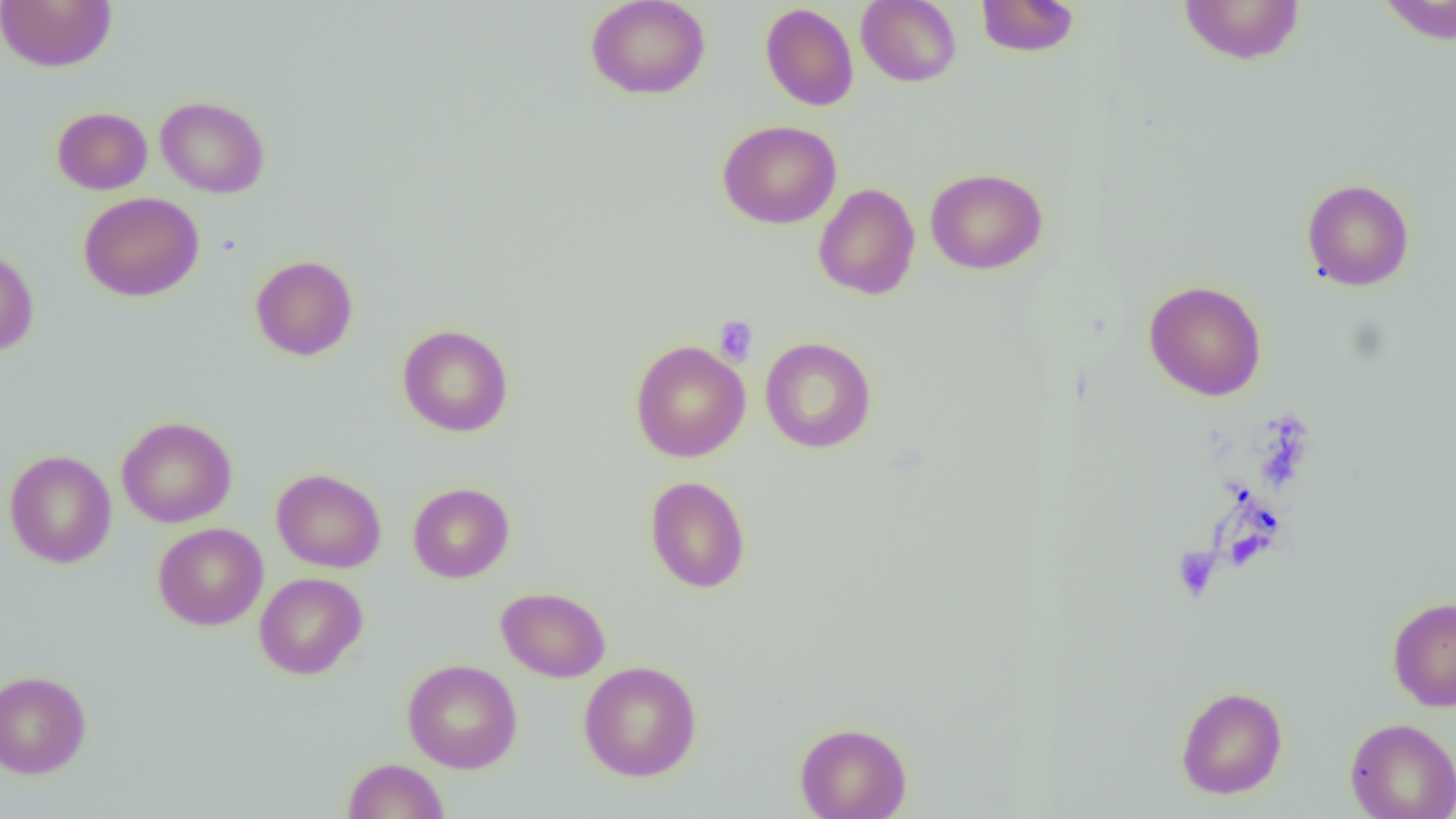 Approximate bounding boxes as (x1, y1, x2, y2) in pixels. Uninfected red blood cell locations: (0, 0, 117, 72), (585, 0, 711, 99), (857, 0, 961, 87), (975, 0, 1081, 57), (1178, 0, 1306, 65), (1376, 1, 1456, 44), (760, 3, 859, 111), (156, 96, 270, 198), (52, 107, 152, 195), (717, 120, 842, 229), (925, 167, 1048, 275), (1302, 178, 1414, 291), (814, 183, 920, 300), (78, 192, 204, 302), (0, 245, 40, 356), (250, 255, 358, 361), (1143, 280, 1267, 401), (397, 323, 514, 437), (759, 336, 876, 453), (630, 339, 750, 462), (116, 416, 237, 528), (4, 450, 117, 568), (271, 468, 386, 573), (645, 476, 751, 593), (407, 482, 515, 583), (153, 523, 268, 630), (254, 572, 367, 679), (496, 586, 611, 682), (1387, 596, 1456, 711), (403, 658, 523, 773), (578, 661, 702, 781), (0, 670, 91, 778), (1176, 686, 1287, 799), (1345, 717, 1456, 819), (794, 722, 912, 819), (343, 758, 450, 819). Platelet locations: (714, 316, 758, 366), (1173, 547, 1220, 601). Slide-level diagnosis: negative for blood parasites. Single field of view. Captured at 1000x magnification. Optical microscopy. Thin blood film. Image is 1456×819 pixels.